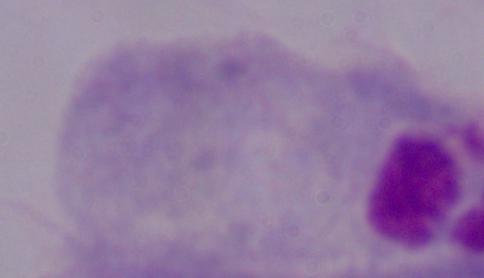

Summary:
  - Magnification: 1000x
  - Modality: micrograph
  - Identification: trichomonad